Comment on the morphology of the erythrocytes.
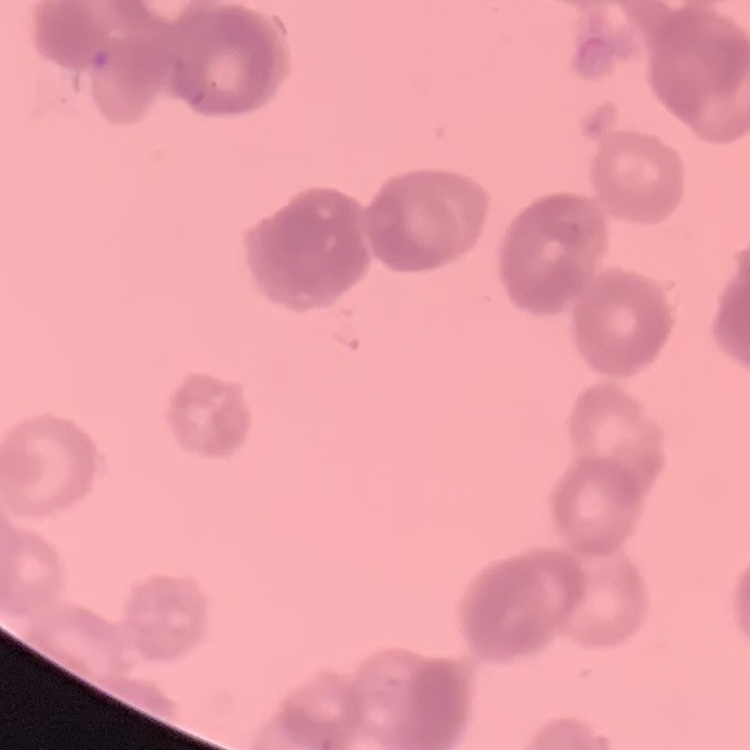

They show rouleaux formation.

preparation = thin peripheral smear
image type = square crop of a larger photomicrograph
stain = Field's or Giemsa